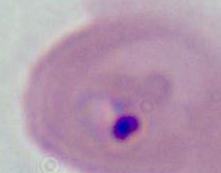
Micrograph. 400x or 1000x magnification. A Plasmodium parasite is shown.